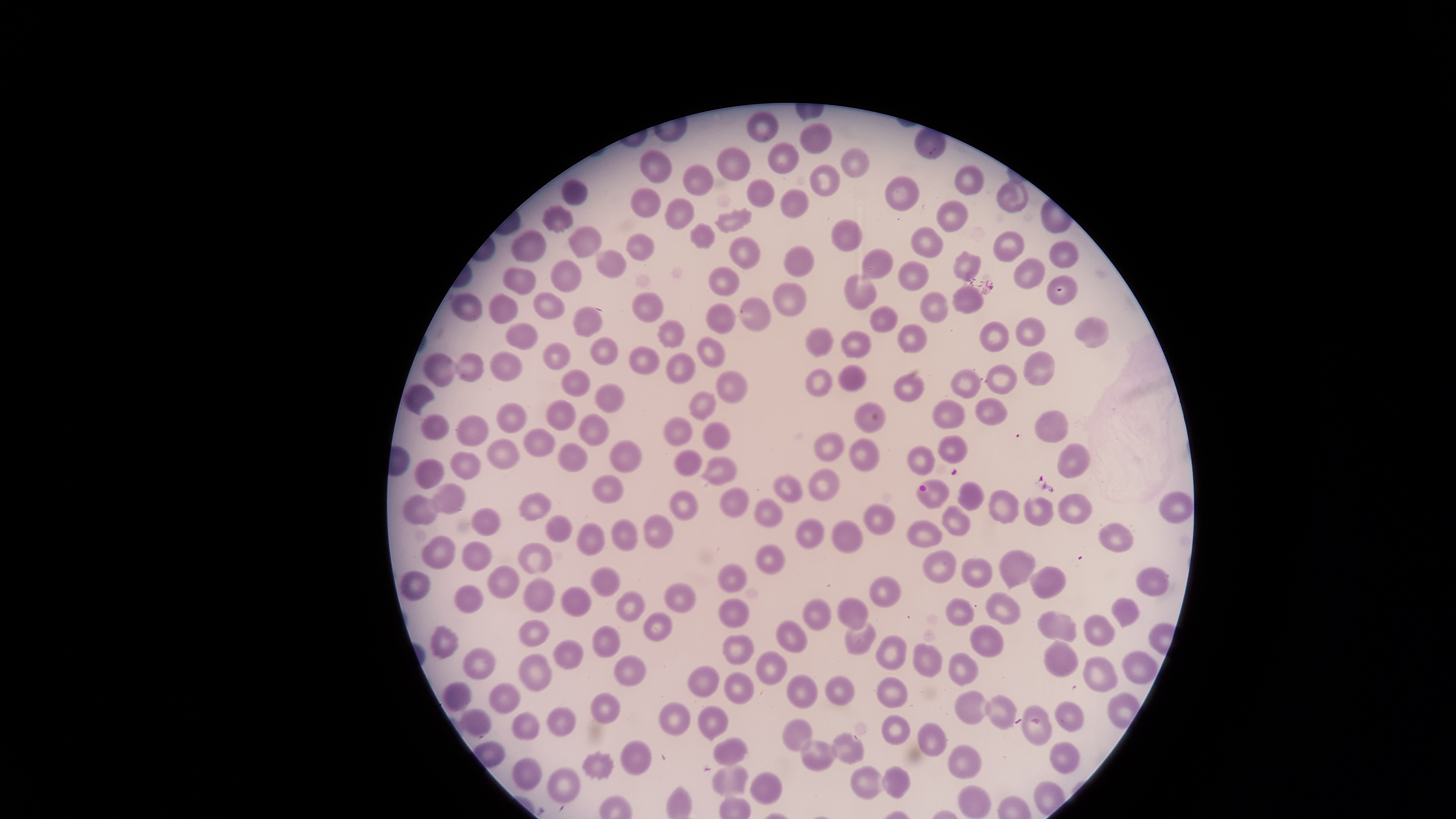

Approximate bounding boxes as (left, top, right, bottom) in pixels. Uninfected red blood cells: (745, 110, 779, 142), (799, 122, 832, 154), (767, 142, 799, 175), (841, 146, 869, 179), (716, 147, 751, 180), (638, 149, 670, 183), (682, 163, 713, 195), (809, 163, 841, 197), (954, 164, 984, 195), (885, 176, 919, 210), (996, 176, 1027, 212), (747, 177, 774, 207), (561, 179, 588, 205), (630, 187, 659, 217), (779, 188, 808, 219), (664, 199, 694, 230), (935, 199, 968, 233), (542, 205, 574, 233), (713, 207, 751, 233), (831, 219, 863, 251), (689, 223, 715, 249), (568, 225, 602, 257), (911, 227, 943, 257), (510, 229, 546, 261), (992, 231, 1024, 262), (626, 233, 655, 263), (727, 235, 759, 269), (1048, 240, 1079, 268), (783, 245, 814, 277), (596, 249, 626, 277), (859, 249, 893, 279), (954, 249, 982, 279), (1012, 258, 1045, 288), (551, 259, 582, 291), (897, 260, 927, 291), (708, 267, 739, 295), (502, 268, 536, 295), (843, 273, 877, 309), (1045, 274, 1077, 306), (772, 281, 806, 317), (952, 287, 983, 313), (634, 291, 662, 323), (919, 291, 948, 323), (451, 293, 482, 321), (532, 293, 564, 319), (488, 295, 518, 325), (739, 297, 769, 331), (705, 303, 736, 334), (572, 305, 602, 337), (869, 305, 897, 333), (1075, 317, 1109, 348), (1015, 318, 1045, 346), (657, 321, 685, 347), (979, 321, 1008, 352), (504, 323, 538, 350), (897, 323, 927, 352), (805, 327, 833, 357), (841, 331, 870, 359), (588, 336, 618, 366), (696, 337, 726, 368), (542, 342, 570, 369), (628, 346, 658, 375), (1024, 350, 1055, 386), (489, 351, 522, 383), (424, 353, 458, 388), (454, 353, 482, 381), (664, 353, 695, 383), (838, 365, 865, 392), (986, 365, 1017, 393), (805, 368, 833, 398), (950, 369, 980, 398), (562, 370, 590, 396), (715, 371, 749, 404), (893, 374, 925, 401), (404, 383, 436, 415), (594, 383, 624, 413), (689, 392, 716, 421), (974, 398, 1006, 426), (544, 399, 576, 430), (933, 400, 965, 429), (496, 403, 527, 434), (855, 403, 885, 433), (1034, 409, 1068, 444), (578, 413, 608, 447), (420, 414, 450, 441), (456, 415, 488, 446), (661, 416, 691, 446), (703, 420, 731, 450), (523, 427, 556, 458), (814, 432, 843, 461), (937, 435, 967, 464), (486, 438, 520, 469), (849, 438, 879, 470), (608, 440, 642, 474), (556, 442, 586, 472), (1057, 444, 1090, 479), (907, 446, 935, 476), (674, 449, 701, 476), (449, 452, 480, 480), (699, 456, 736, 486), (414, 459, 443, 488), (807, 467, 841, 500), (592, 474, 624, 504), (773, 474, 802, 504), (917, 479, 948, 508), (957, 480, 983, 511), (428, 483, 465, 513), (719, 487, 749, 518), (987, 489, 1018, 523), (669, 490, 697, 520), (1158, 491, 1193, 523), (518, 492, 552, 520), (1058, 493, 1092, 525), (401, 494, 439, 525), (1023, 496, 1053, 526), (754, 498, 783, 526), (863, 504, 895, 535), (942, 506, 969, 536), (472, 508, 500, 535), (642, 514, 673, 548), (544, 515, 572, 542), (610, 518, 637, 552), (795, 518, 824, 550), (831, 520, 863, 554), (907, 520, 940, 548), (576, 522, 604, 557), (1098, 523, 1134, 553), (421, 535, 455, 569), (462, 541, 491, 570), (518, 543, 552, 573), (923, 550, 956, 582), (998, 550, 1034, 594), (961, 558, 992, 588), (488, 565, 518, 599), (1030, 566, 1066, 600), (590, 568, 620, 596), (1135, 568, 1168, 598), (398, 570, 429, 601), (523, 578, 554, 613), (453, 584, 482, 615), (663, 584, 695, 612), (559, 586, 591, 617), (616, 590, 645, 622), (984, 592, 1021, 626), (837, 596, 868, 632), (1111, 596, 1140, 630), (801, 598, 831, 632), (945, 598, 974, 626), (1036, 610, 1077, 642), (1084, 614, 1116, 646), (517, 619, 549, 645), (775, 620, 807, 653), (845, 620, 875, 654), (968, 624, 1003, 657), (429, 625, 458, 659), (592, 626, 620, 658), (721, 634, 753, 664), (875, 636, 907, 671), (553, 639, 583, 669), (1043, 639, 1078, 677), (911, 642, 941, 678), (462, 647, 495, 679), (754, 650, 787, 686), (1122, 650, 1158, 686), (948, 652, 979, 686), (517, 653, 551, 693), (614, 656, 645, 687), (1082, 656, 1118, 693), (687, 666, 719, 697), (724, 672, 753, 704), (786, 675, 819, 709), (875, 677, 907, 709), (442, 683, 472, 711), (488, 683, 519, 713), (954, 691, 991, 726), (592, 693, 620, 723), (986, 695, 1017, 729), (659, 702, 689, 736), (1055, 702, 1082, 732), (697, 705, 727, 742), (1021, 705, 1052, 745), (547, 707, 575, 736), (460, 709, 492, 738), (511, 713, 539, 739), (880, 715, 909, 745), (781, 719, 813, 751), (917, 723, 946, 757), (830, 731, 864, 765), (713, 738, 748, 765), (799, 739, 838, 771), (620, 740, 650, 777), (1049, 741, 1080, 775), (948, 745, 982, 779), (581, 751, 614, 781), (512, 757, 541, 791), (712, 765, 749, 797), (547, 767, 580, 803), (848, 767, 888, 799), (882, 767, 910, 799), (749, 771, 783, 805), (956, 787, 990, 817). Photographed with a smartphone camera through the microscope eyepiece. Giemsa stain. The visible region is circular. Presence: no malaria parasites detected. Single field of view. Image is 1456×819 pixels. Thin blood film.